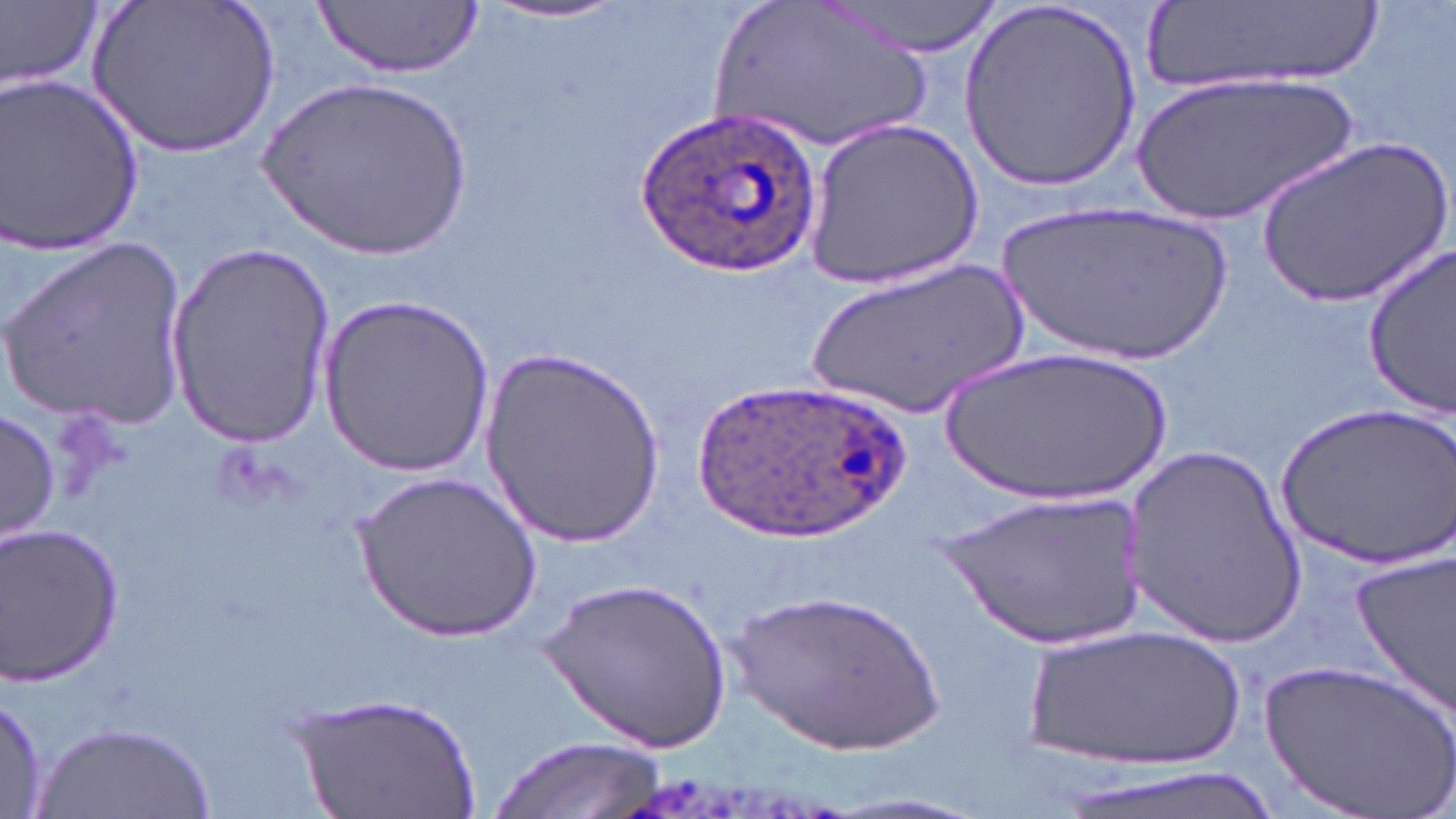
{
  "slide_level_diagnosis": "Plasmodium ovale",
  "field_of_view": "one of a larger specimen",
  "preparation": "thin blood smear",
  "image_size": "1456×819 pixels",
  "stain": "May-Grünwald-Giemsa",
  "magnification": "1000x",
  "modality": "light microscopy",
  "plasmodium_ovale_infected_red_blood_cell_locations": "approximate bounding boxes as (x1, y1, x2, y2) in pixels: (641, 110, 816, 274), (689, 378, 910, 543)",
  "uninfected_red_blood_cell_locations": "approximate bounding boxes as (x1, y1, x2, y2) in pixels: (82, 0, 286, 159), (314, 0, 482, 79), (709, 0, 940, 155), (825, 0, 1009, 58), (1, 1, 102, 93), (957, 1, 1143, 194), (473, 2, 637, 28), (1141, 4, 1377, 96), (0, 68, 148, 258), (1133, 71, 1364, 227), (258, 76, 478, 266), (804, 119, 984, 289), (1259, 134, 1449, 306), (992, 197, 1237, 369), (4, 234, 192, 428), (165, 239, 337, 449), (1362, 243, 1456, 413), (802, 254, 1033, 422), (321, 293, 493, 480), (936, 345, 1180, 505), (480, 350, 665, 547), (1277, 400, 1452, 566), (0, 407, 59, 545), (1122, 441, 1309, 643), (353, 471, 548, 643), (943, 487, 1145, 649), (0, 521, 127, 687), (1349, 547, 1456, 723), (541, 578, 732, 753), (730, 586, 950, 757), (1017, 620, 1250, 771), (1259, 657, 1456, 819), (0, 687, 50, 819), (290, 691, 483, 819), (34, 721, 218, 819), (490, 735, 666, 819), (1049, 762, 1286, 819)"
}